Assess this cell for malaria.
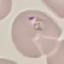
Parasitized.

Automatically extracted cell patch, resized to 64 × 64 pixels. Giemsa-stained preparation. Photographed with a smartphone camera at the microscope eyepiece. Thin smear of blood.